Evaluate for Plasmodium parasites.
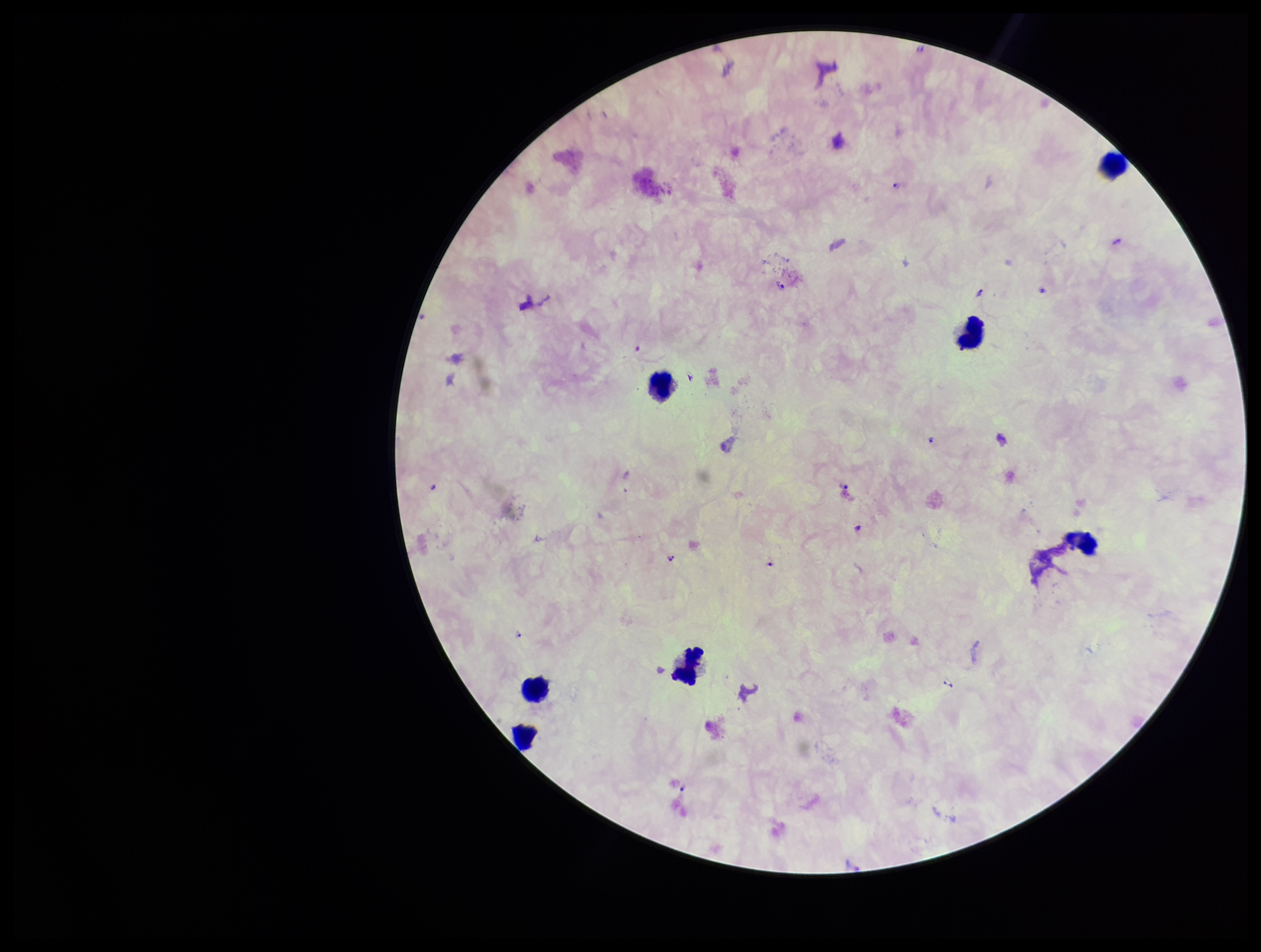

Seen.

capture = smartphone photograph through the microscope eyepiece
stain = Giemsa
parasite count = 15
species reported for this patient = Plasmodium falciparum
leukocyte count = 7
image size = 1261×952 pixels
preparation = thick
patient malaria status = infected
field of view = one from this slide